Evaluate for Plasmodium parasites.
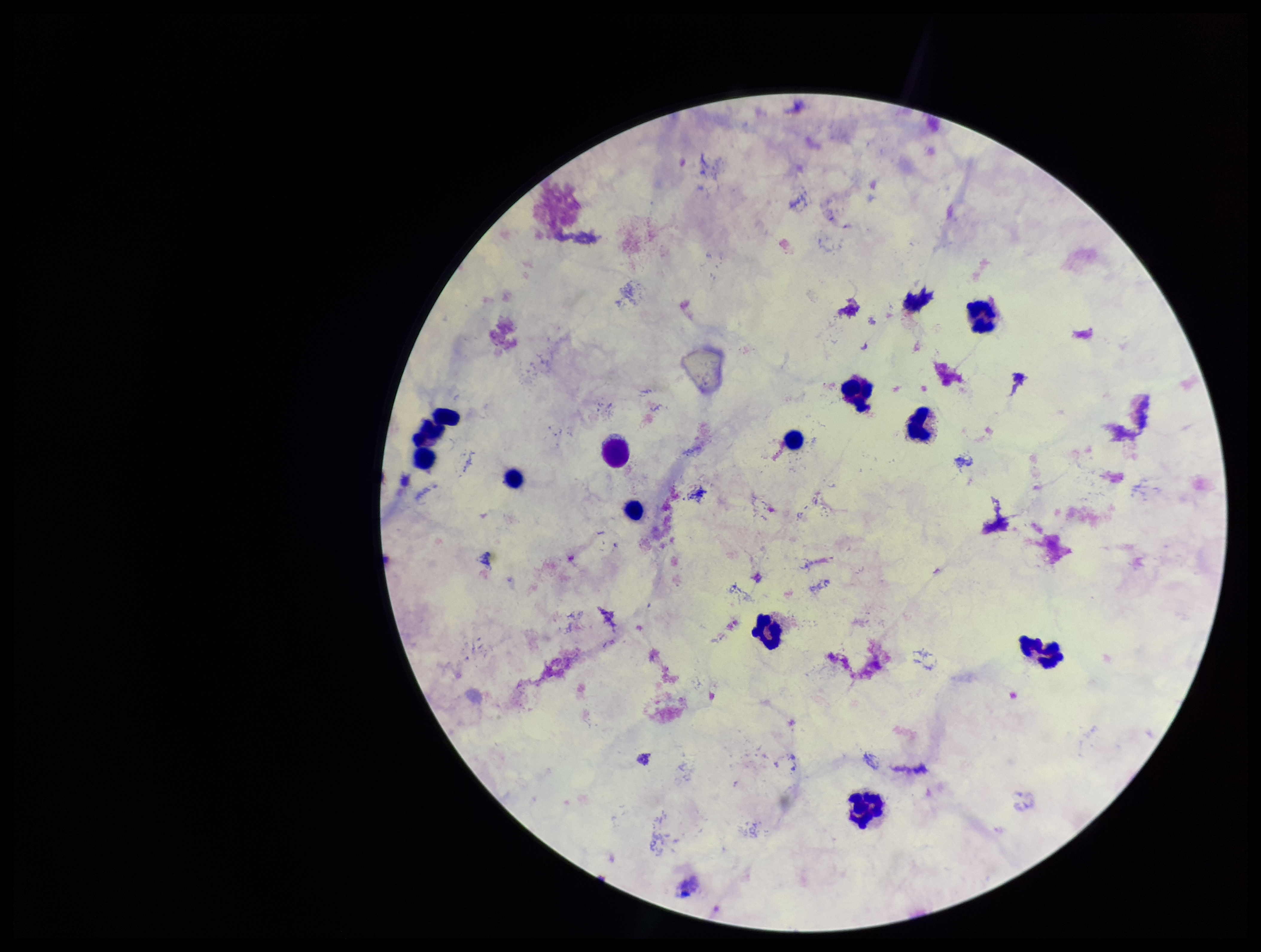
None identified.

leukocyte count = 12
image size = 1261×952 pixels
stain = Giemsa
capture = smartphone photograph through the microscope eyepiece
field of view = one from this slide
preparation = thick smear
parasite count = 0
patient malaria status = negative